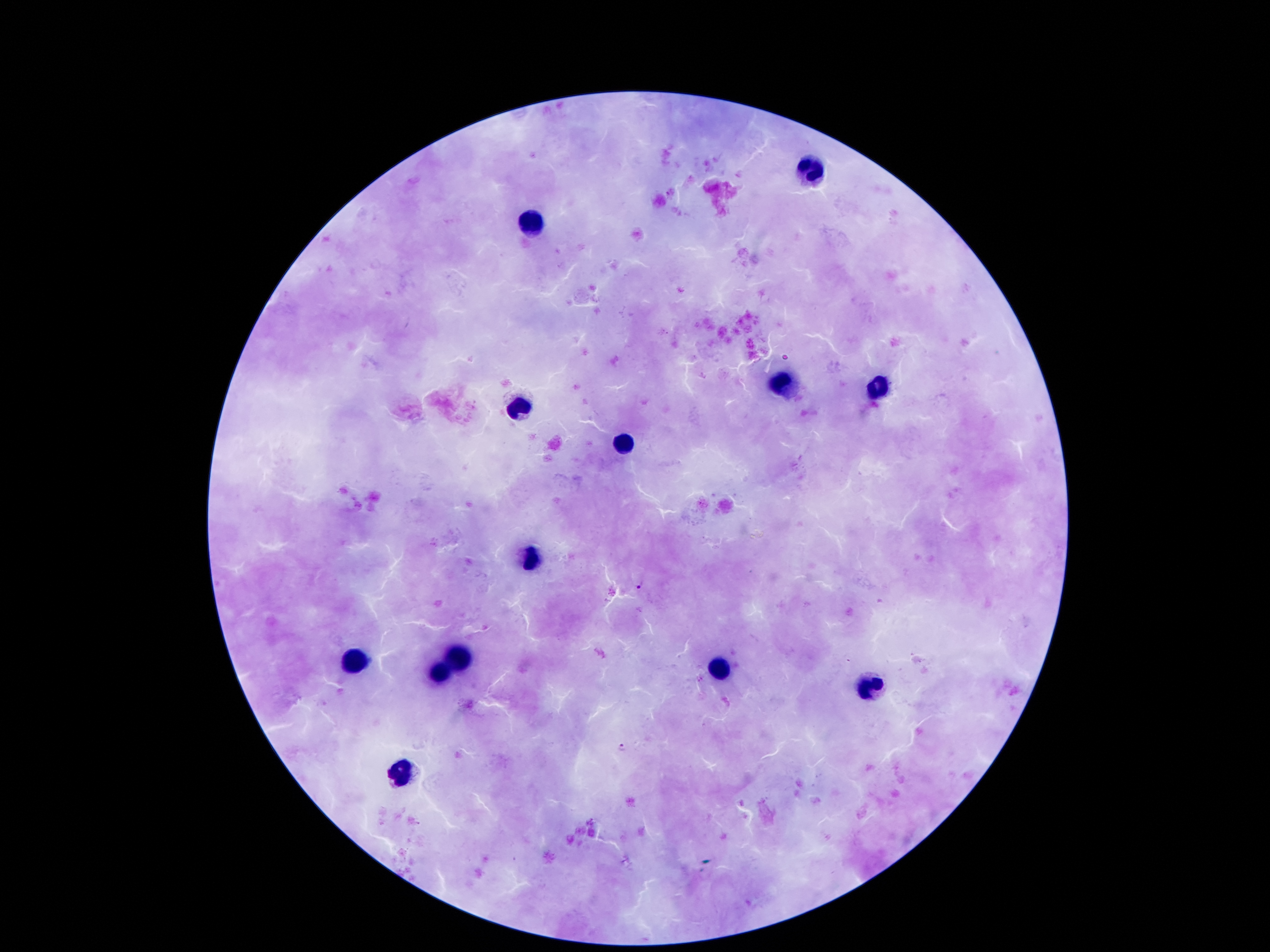

Approximate object centers, in pixels from the top-left corner.
Summary:
  - Malaria parasite locations: (x=638, y=584), (x=621, y=746)
  - Leukocyte locations: (x=810, y=173), (x=535, y=223), (x=784, y=388), (x=881, y=388), (x=519, y=405), (x=625, y=443), (x=532, y=557), (x=464, y=652), (x=354, y=662), (x=718, y=670), (x=440, y=673), (x=869, y=691), (x=402, y=775)
  - Capture: smartphone through the microscope eyepiece
  - Preparation: thick blood film
  - Field of view: one from this slide
  - Stain: Giemsa
  - Magnification: 100x
  - Patient malaria status: infected with Plasmodium falciparum
  - Image size: 1270×952 pixels